Assess the morphology of the red blood cells.
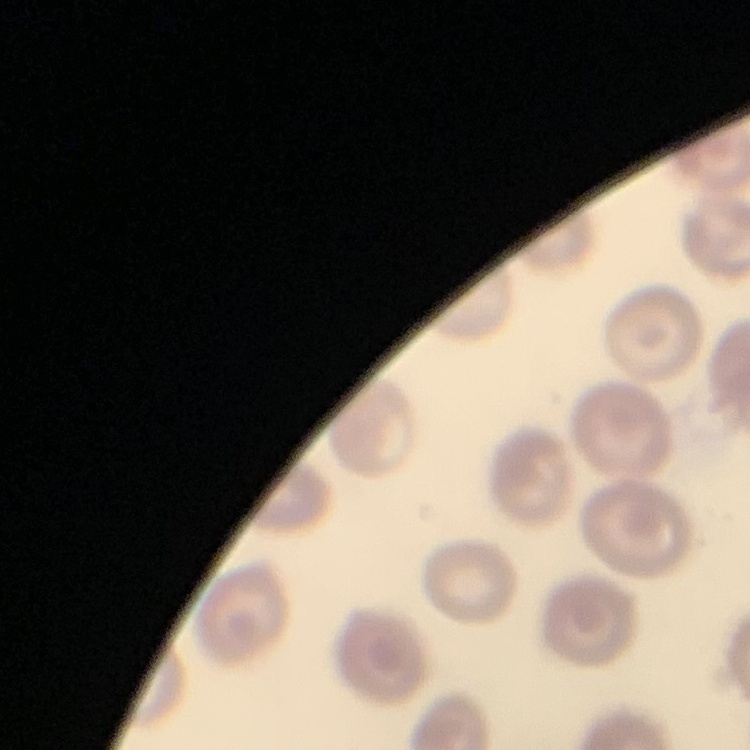

They show no rouleaux formation.

Square crop of a larger photomicrograph. Thin blood smear. Field's or Giemsa stain.